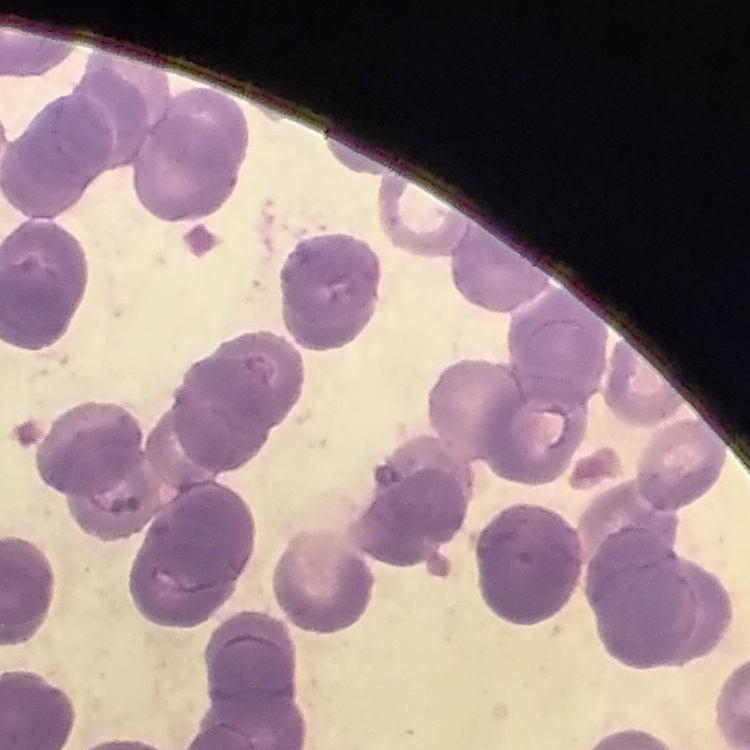
The red blood cells exhibit rouleaux formation. Thin peripheral smear. One tile cut from a larger photomicrograph. Stained with either Field's or Giemsa.